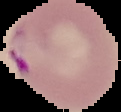

image size = 121×112 pixels
image type = cell region segmented out of the field of view; surrounding area masked to black
preparation = thin blood film
result = malaria parasites detected